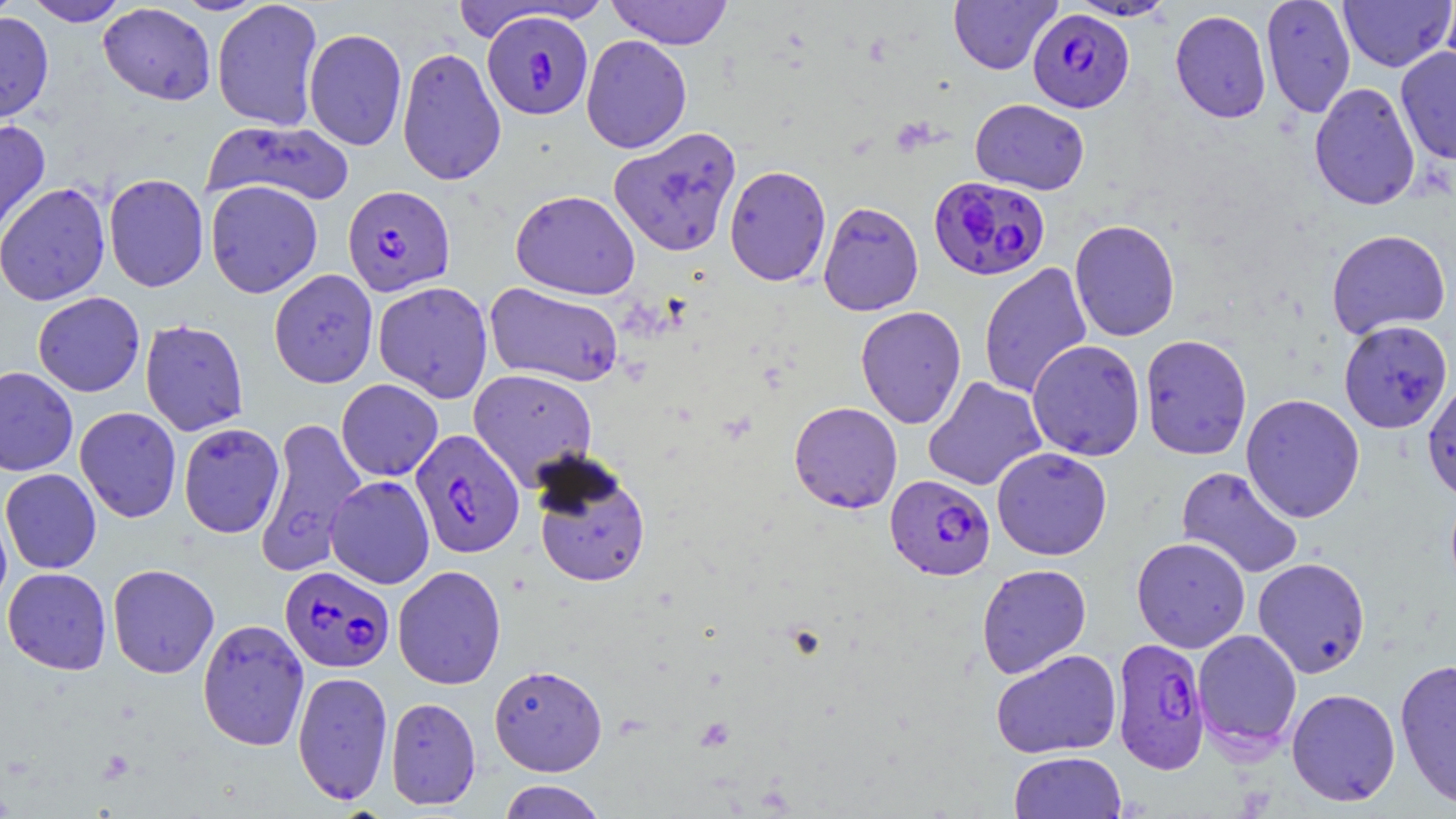
Summary:
  - Coordinate format: approximate bounding boxes as named x1/y1/x2/y2 corners in pixels
  - Plasmodium falciparum-infected red blood cell locations: (x1=1027, y1=8, x2=1134, y2=113), (x1=482, y1=11, x2=594, y2=120), (x1=929, y1=175, x2=1051, y2=281), (x1=342, y1=185, x2=455, y2=296), (x1=410, y1=429, x2=525, y2=559), (x1=885, y1=475, x2=995, y2=580), (x1=280, y1=565, x2=394, y2=673), (x1=1111, y1=637, x2=1210, y2=774)
  - Uninfected red blood cell locations: (x1=0, y1=0, x2=21, y2=23), (x1=24, y1=0, x2=130, y2=26), (x1=172, y1=0, x2=267, y2=15), (x1=211, y1=0, x2=324, y2=131), (x1=606, y1=0, x2=733, y2=49), (x1=948, y1=0, x2=1060, y2=74), (x1=1067, y1=0, x2=1177, y2=21), (x1=1260, y1=0, x2=1356, y2=118), (x1=1338, y1=0, x2=1455, y2=72), (x1=1440, y1=0, x2=1456, y2=81), (x1=447, y1=1, x2=593, y2=42), (x1=98, y1=3, x2=216, y2=105), (x1=1170, y1=10, x2=1272, y2=123), (x1=0, y1=12, x2=54, y2=123), (x1=303, y1=28, x2=407, y2=151), (x1=581, y1=35, x2=692, y2=153), (x1=396, y1=46, x2=506, y2=186), (x1=1396, y1=46, x2=1456, y2=165), (x1=1309, y1=82, x2=1421, y2=211), (x1=970, y1=98, x2=1090, y2=195), (x1=0, y1=119, x2=51, y2=247), (x1=202, y1=119, x2=354, y2=209), (x1=609, y1=126, x2=742, y2=257), (x1=724, y1=165, x2=832, y2=287), (x1=104, y1=173, x2=209, y2=292), (x1=205, y1=180, x2=323, y2=298), (x1=0, y1=182, x2=111, y2=306), (x1=510, y1=189, x2=640, y2=299), (x1=817, y1=201, x2=924, y2=316), (x1=1069, y1=219, x2=1181, y2=341), (x1=1325, y1=229, x2=1451, y2=339), (x1=978, y1=262, x2=1092, y2=399), (x1=268, y1=269, x2=378, y2=388), (x1=373, y1=281, x2=493, y2=403), (x1=484, y1=283, x2=625, y2=388), (x1=32, y1=292, x2=145, y2=397), (x1=855, y1=305, x2=967, y2=429), (x1=140, y1=319, x2=249, y2=436), (x1=1338, y1=320, x2=1453, y2=434), (x1=1139, y1=334, x2=1252, y2=460), (x1=1026, y1=339, x2=1146, y2=461), (x1=0, y1=366, x2=78, y2=477), (x1=468, y1=368, x2=598, y2=489), (x1=923, y1=376, x2=1046, y2=491), (x1=1422, y1=376, x2=1456, y2=504), (x1=336, y1=379, x2=443, y2=481), (x1=1241, y1=393, x2=1365, y2=523), (x1=789, y1=401, x2=903, y2=513), (x1=75, y1=407, x2=182, y2=523), (x1=254, y1=417, x2=366, y2=576), (x1=179, y1=422, x2=285, y2=538), (x1=991, y1=447, x2=1112, y2=561), (x1=532, y1=456, x2=651, y2=588), (x1=1176, y1=465, x2=1304, y2=580), (x1=0, y1=469, x2=102, y2=574), (x1=325, y1=475, x2=435, y2=589), (x1=0, y1=499, x2=12, y2=613), (x1=1131, y1=536, x2=1250, y2=652), (x1=1252, y1=557, x2=1371, y2=678), (x1=107, y1=563, x2=220, y2=678), (x1=976, y1=563, x2=1091, y2=678), (x1=392, y1=565, x2=507, y2=689), (x1=3, y1=567, x2=112, y2=675), (x1=197, y1=618, x2=310, y2=751), (x1=1193, y1=629, x2=1302, y2=754), (x1=990, y1=649, x2=1122, y2=759), (x1=1395, y1=658, x2=1456, y2=809), (x1=488, y1=664, x2=607, y2=776), (x1=292, y1=670, x2=393, y2=805), (x1=1286, y1=688, x2=1401, y2=806), (x1=385, y1=696, x2=481, y2=810), (x1=1009, y1=751, x2=1127, y2=819), (x1=498, y1=780, x2=607, y2=819)
  - Slide-level diagnosis: Plasmodium falciparum
  - Stain: May-Grünwald-Giemsa
  - Preparation: thin blood film
  - Modality: light microscopy
  - Magnification: 1000x
  - Field of view: single
  - Image size: 1456×819 pixels